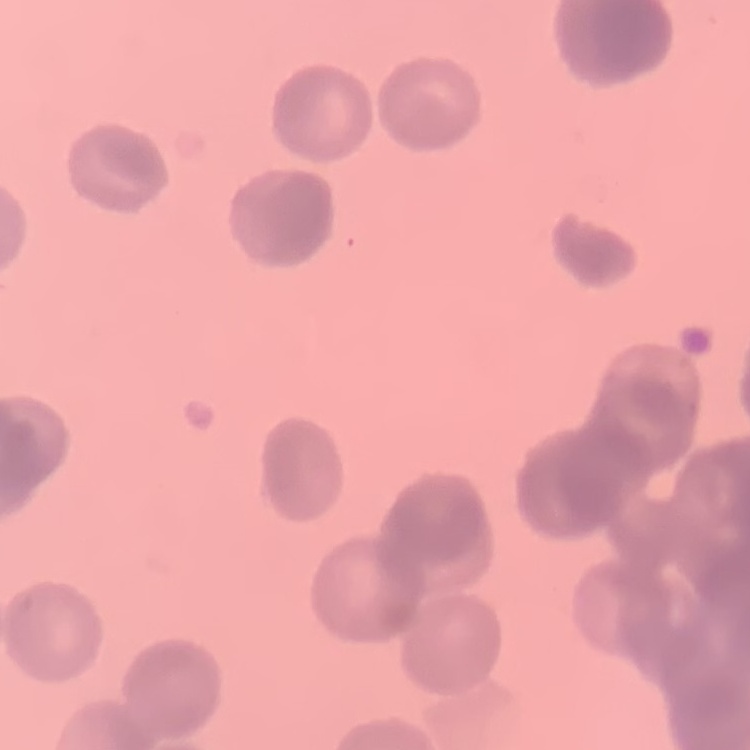

The erythrocytes exhibit rouleaux formation. Thin peripheral smear. Field's or Giemsa stain. Square crop of a larger photomicrograph.